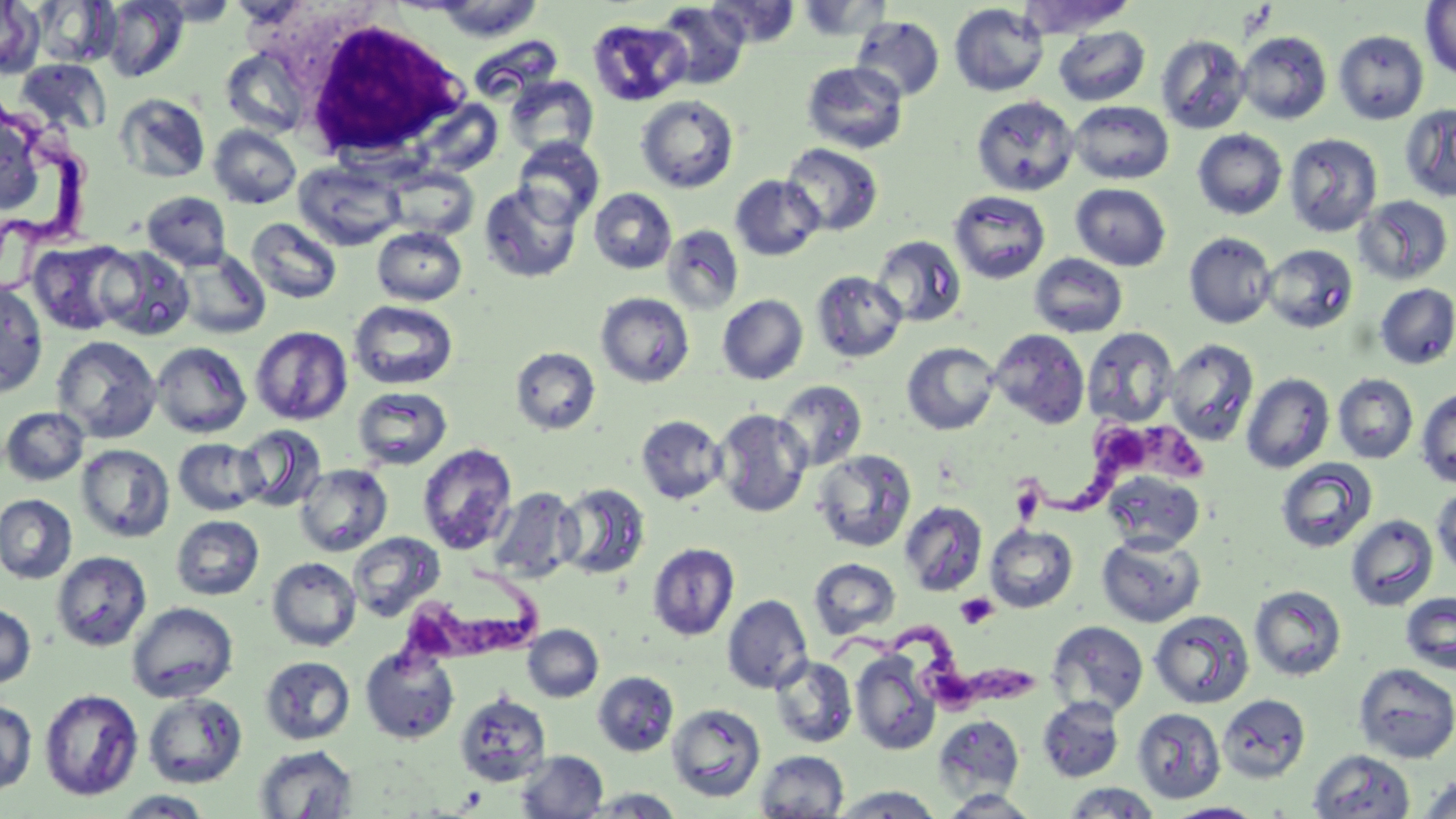

Summary:
  - Coordinate format: approximate bounding boxes as (x1, y1, x2, y2) in pixels
  - Uninfected red blood cell locations: (32, 0, 120, 67), (99, 0, 189, 82), (153, 0, 242, 25), (1017, 0, 1136, 38), (0, 1, 45, 78), (706, 1, 801, 48), (795, 1, 892, 41), (1421, 1, 1455, 81), (652, 2, 750, 89), (949, 3, 1049, 96), (850, 15, 945, 102), (587, 19, 691, 106), (1054, 27, 1150, 106), (1334, 30, 1428, 124), (1238, 31, 1332, 124), (1156, 34, 1251, 134), (220, 50, 308, 136), (16, 59, 112, 135), (801, 61, 908, 154), (505, 75, 599, 161), (113, 93, 211, 184), (636, 95, 739, 193), (971, 95, 1080, 197), (1068, 101, 1174, 184), (1400, 104, 1456, 203), (0, 115, 47, 217), (209, 125, 302, 208), (1193, 129, 1287, 220), (1285, 133, 1382, 237), (512, 137, 604, 227), (781, 143, 883, 237), (294, 160, 407, 251), (383, 166, 479, 240), (730, 175, 825, 261), (478, 183, 583, 283), (1071, 183, 1171, 271), (589, 188, 677, 274), (948, 190, 1051, 284), (141, 191, 232, 270), (1355, 195, 1453, 285), (245, 217, 342, 304), (662, 224, 745, 315), (372, 226, 467, 306), (1183, 232, 1278, 329), (871, 234, 967, 328), (28, 240, 135, 335), (1262, 244, 1358, 333), (97, 246, 196, 341), (174, 249, 270, 339), (1030, 253, 1128, 338), (811, 271, 908, 363), (0, 280, 49, 400), (1375, 283, 1456, 369), (595, 292, 694, 387), (717, 294, 808, 385), (349, 300, 458, 389), (250, 326, 353, 425), (1082, 327, 1178, 427), (989, 328, 1090, 429), (51, 335, 162, 443), (1164, 338, 1259, 447), (151, 341, 252, 438), (902, 342, 1001, 435), (510, 347, 601, 436), (1241, 373, 1335, 473), (1332, 374, 1419, 464), (774, 380, 867, 472), (353, 386, 452, 470), (1416, 387, 1456, 488), (1, 406, 89, 486), (713, 408, 812, 517), (636, 415, 727, 504), (234, 424, 327, 512), (173, 438, 266, 516), (417, 443, 517, 556), (76, 444, 175, 543), (812, 450, 916, 553), (1275, 458, 1378, 553), (295, 464, 393, 556), (1101, 470, 1205, 552), (556, 483, 650, 580), (1432, 484, 1456, 576), (488, 487, 582, 583), (0, 494, 77, 585), (899, 501, 987, 596), (1345, 514, 1438, 611), (171, 515, 264, 600), (985, 524, 1078, 613), (347, 532, 445, 622), (1096, 534, 1206, 627), (648, 542, 740, 640), (51, 551, 151, 651), (267, 557, 362, 651), (809, 558, 901, 639), (1249, 585, 1347, 681), (1400, 592, 1456, 674), (722, 594, 813, 694), (127, 602, 238, 703), (0, 603, 36, 690), (1149, 610, 1254, 709), (1047, 620, 1149, 718), (523, 624, 603, 702), (360, 645, 460, 744), (850, 651, 941, 755), (260, 655, 355, 745), (770, 655, 857, 748), (1354, 663, 1456, 763), (593, 672, 678, 757), (39, 689, 143, 801), (454, 690, 551, 786), (143, 693, 247, 788), (1217, 693, 1311, 782), (1037, 697, 1124, 782), (0, 698, 38, 795), (668, 703, 766, 801), (1132, 707, 1225, 803), (933, 715, 1025, 799), (254, 744, 358, 818), (1308, 749, 1416, 819), (514, 750, 608, 818), (754, 750, 849, 818), (1417, 775, 1456, 819), (1060, 783, 1163, 818), (827, 785, 946, 818), (580, 788, 686, 817), (939, 789, 1045, 817), (111, 790, 215, 818), (1165, 803, 1266, 819)
  - White blood cell locations: (292, 15, 469, 162)
  - Trypanosoma brucei locations: (1, 108, 99, 251), (1044, 411, 1223, 523), (391, 558, 552, 682), (827, 625, 1046, 707)
  - Platelet locations: (1010, 482, 1045, 525), (955, 592, 998, 629)
  - Slide-level diagnosis: Trypanosoma brucei
  - Preparation: thin blood smear
  - Magnification: 1000x
  - Field of view: one of a larger specimen
  - Stain: May-Grünwald-Giemsa
  - Modality: light microscopy
  - Image size: 1456×819 pixels